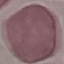
malaria status = uninfected
capture = smartphone through the microscope eyepiece
stain = Giemsa
preparation = thin blood smear
image type = automatically extracted cell patch, resized to 64 × 64 pixels